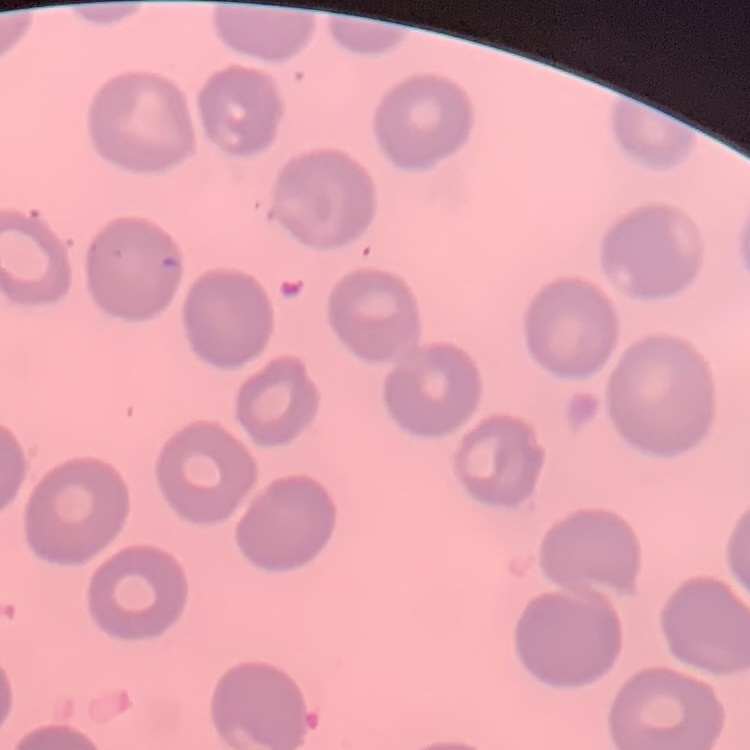
The erythrocytes show no rouleaux formation. Field's or Giemsa stain. One tile cut from a larger photomicrograph. Thin peripheral smear.